Assess this cell for malaria.
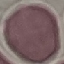
Uninfected.

Acquired by smartphone through the microscope eyepiece. Cell patch, automatically extracted from a larger field of view and resized to 64 × 64 pixels. Thin blood film. Giemsa-stained preparation.